State the preparation type.
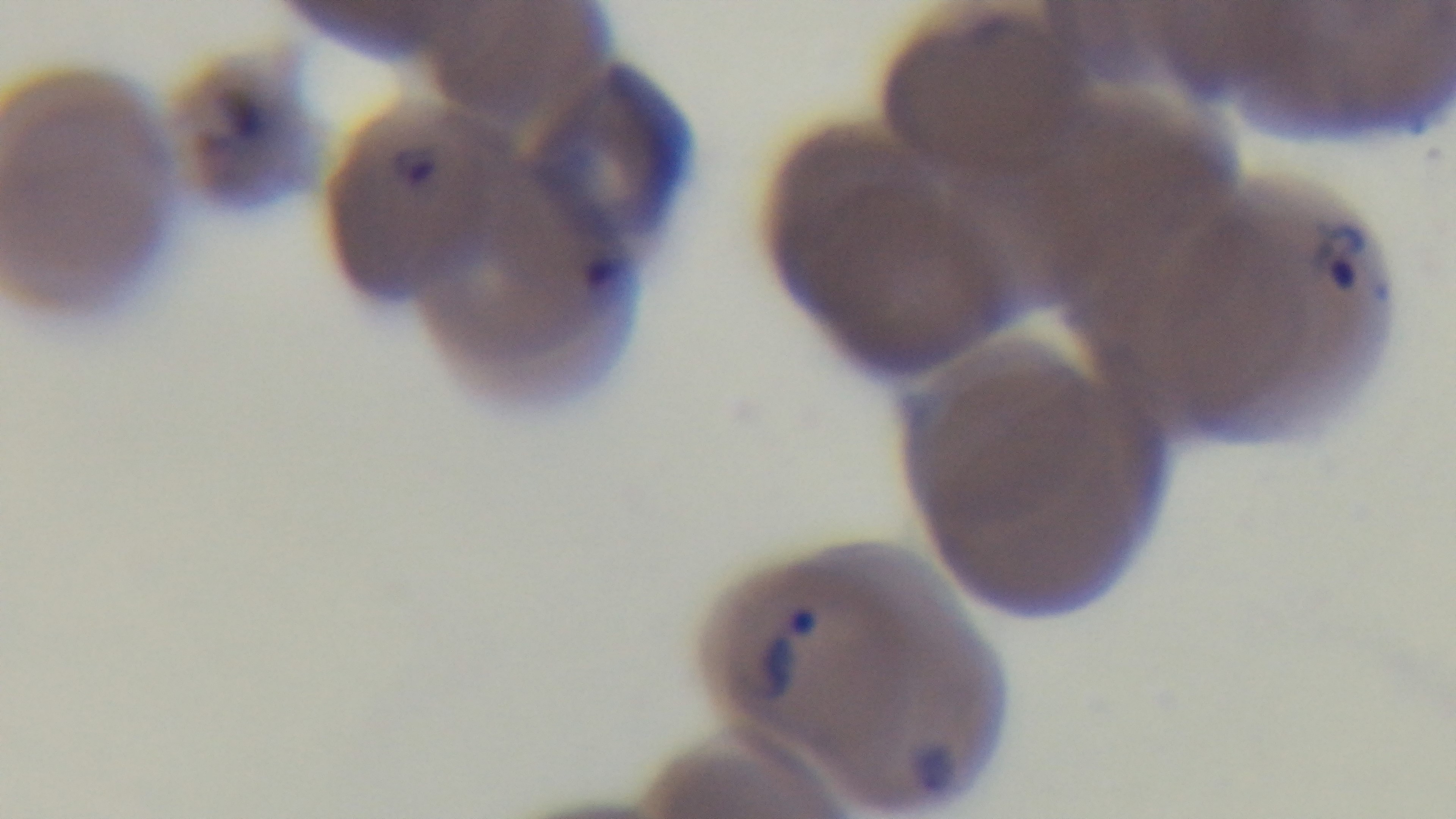

Thin.

modality = light microscopy
capture = mounted 4K digital camera
malaria status = positive
stain = Giemsa
field of view = single
objective = 100x oil immersion